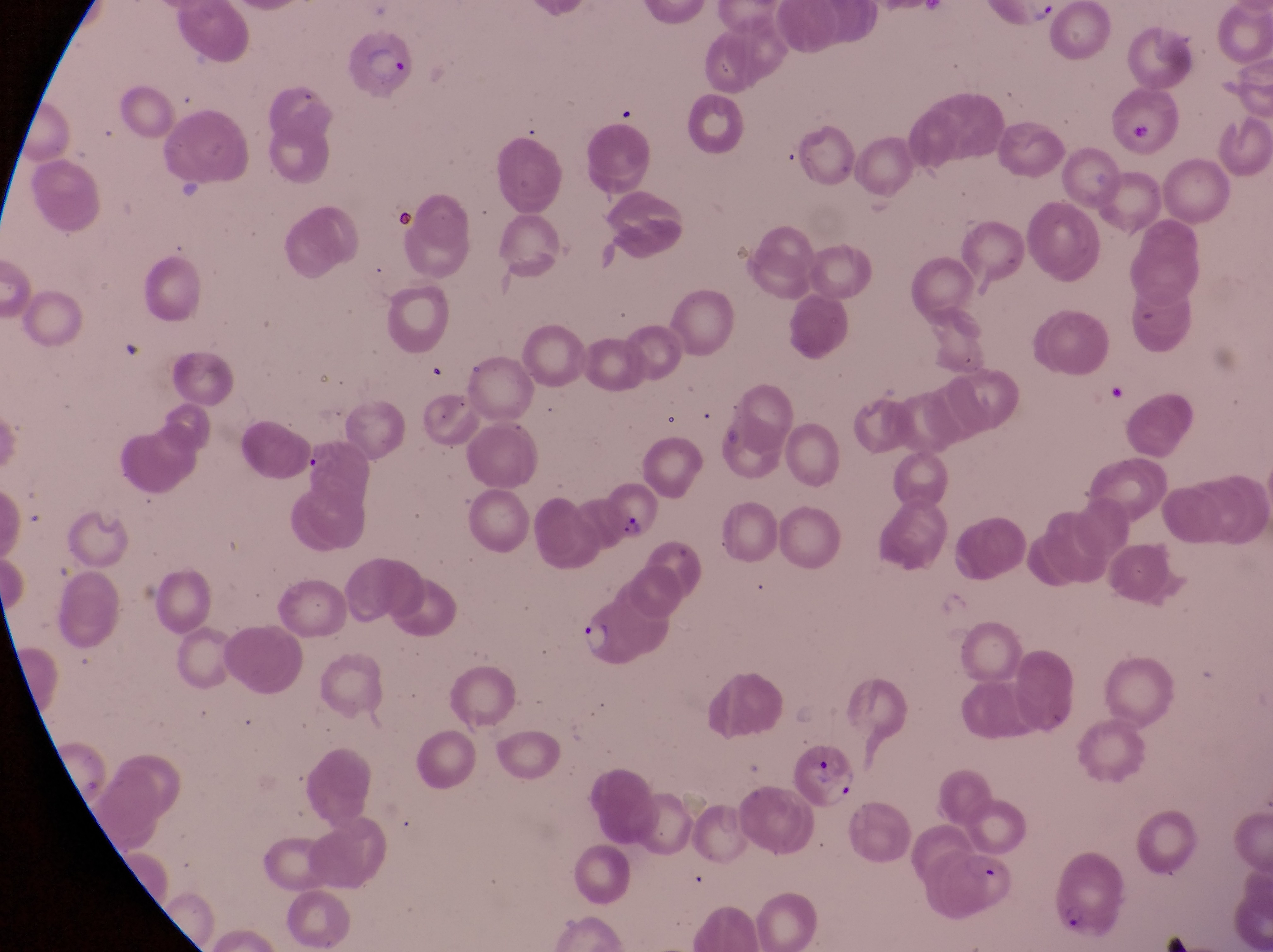

Approximate bounding boxes as [left, top, right, bottom] in pixels. Parasitised red blood cell locations: [345, 30, 419, 100], [599, 479, 661, 544], [794, 741, 857, 808], [1046, 844, 1123, 936], [929, 851, 1019, 921]. Trophozoite locations: [576, 624, 618, 659]. Captured by a smartphone held over the eyepiece of an Olympus CX-23 microscope. Image is 1273×952 pixels. Magnification of 1000x. Sample from Uganda. One field of view. Thin blood smear.